Report the malaria status of this cell.
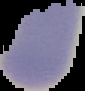

Uninfected.

image_type: segmented cell region with the area outside set to black
preparation: thin blood film
image_size: 85×91 pixels